Report the malaria status of this cell.
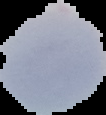
Uninfected.

Summary:
  - Image size: 106×115 pixels
  - Image type: segmented cell region with the area outside set to black
  - Preparation: thin blood smear